State which cell type is depicted.
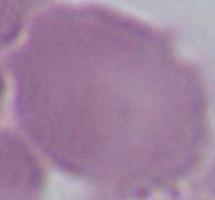

An erythrocyte.

Photomicrograph. Captured at 1000x magnification.